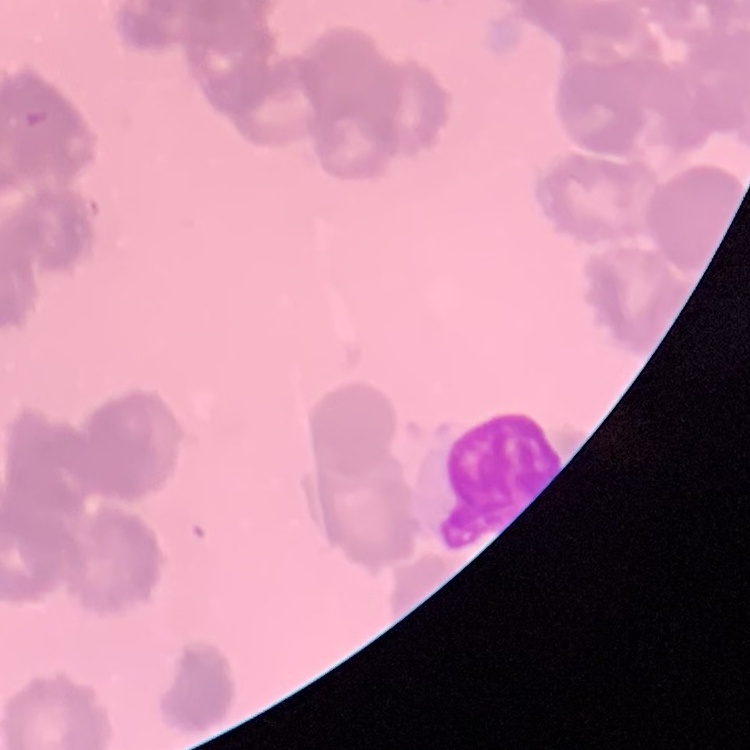
red blood cell morphology = rouleaux formation
image type = square crop of a larger photomicrograph
stain = Field's or Giemsa
preparation = thin peripheral smear